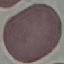

Result: no malaria parasites seen. Giemsa-stained preparation. Acquired by smartphone through the microscope eyepiece. Cell patch, automatically extracted from a larger field of view and resized to 64 × 64 pixels. Thin blood film.